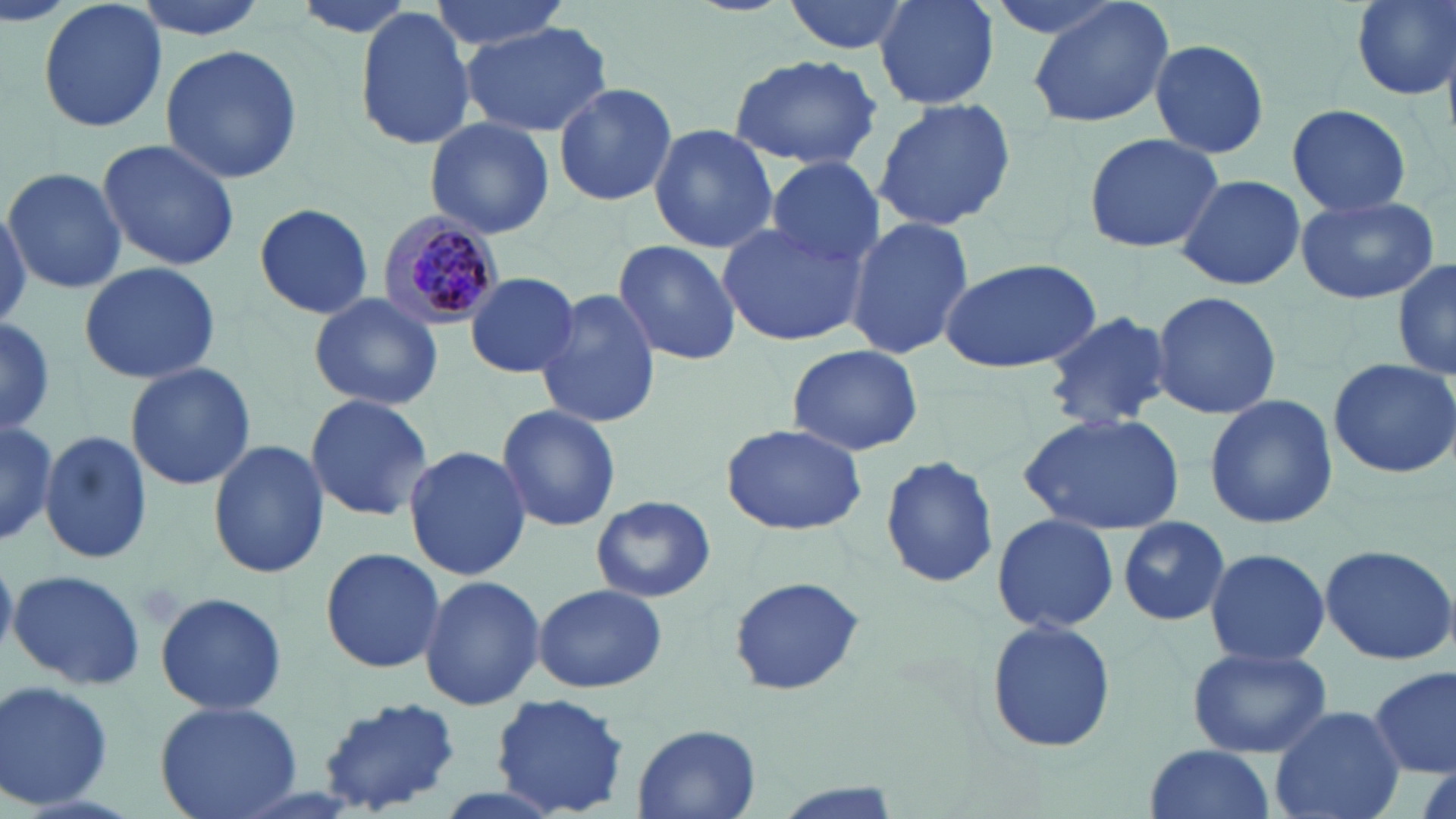
slide-level diagnosis = Plasmodium malariae
field of view = single
modality = optical microscopy
uninfected red blood cell locations = approximate bounding boxes as named x1/y1/x2/y2 corners in pixels: (x1=38, y1=0, x2=167, y2=133), (x1=128, y1=0, x2=272, y2=41), (x1=424, y1=0, x2=571, y2=51), (x1=784, y1=0, x2=912, y2=55), (x1=873, y1=0, x2=1000, y2=109), (x1=1027, y1=0, x2=1176, y2=131), (x1=1352, y1=0, x2=1455, y2=99), (x1=353, y1=9, x2=480, y2=149), (x1=461, y1=24, x2=612, y2=138), (x1=1147, y1=38, x2=1270, y2=159), (x1=159, y1=44, x2=304, y2=182), (x1=729, y1=53, x2=882, y2=170), (x1=551, y1=82, x2=678, y2=208), (x1=873, y1=97, x2=1017, y2=231), (x1=1284, y1=104, x2=1414, y2=218), (x1=424, y1=118, x2=555, y2=241), (x1=648, y1=123, x2=777, y2=252), (x1=1083, y1=131, x2=1225, y2=253), (x1=96, y1=137, x2=240, y2=272), (x1=764, y1=155, x2=883, y2=271), (x1=4, y1=168, x2=125, y2=293), (x1=1175, y1=174, x2=1306, y2=292), (x1=1296, y1=193, x2=1440, y2=305), (x1=0, y1=203, x2=31, y2=328), (x1=254, y1=203, x2=373, y2=319), (x1=845, y1=215, x2=974, y2=360), (x1=716, y1=220, x2=867, y2=348), (x1=613, y1=239, x2=740, y2=366), (x1=939, y1=256, x2=1101, y2=375), (x1=1393, y1=258, x2=1456, y2=383), (x1=77, y1=262, x2=222, y2=385), (x1=465, y1=272, x2=578, y2=377), (x1=535, y1=288, x2=664, y2=432), (x1=1150, y1=289, x2=1282, y2=421), (x1=308, y1=291, x2=445, y2=410), (x1=1043, y1=309, x2=1174, y2=429), (x1=0, y1=318, x2=59, y2=435), (x1=785, y1=345, x2=925, y2=457), (x1=1326, y1=357, x2=1456, y2=479), (x1=123, y1=361, x2=257, y2=491), (x1=1204, y1=392, x2=1339, y2=529), (x1=304, y1=393, x2=436, y2=521), (x1=496, y1=405, x2=622, y2=534), (x1=1021, y1=411, x2=1185, y2=534), (x1=719, y1=423, x2=870, y2=536), (x1=38, y1=428, x2=152, y2=569), (x1=207, y1=439, x2=328, y2=579), (x1=403, y1=445, x2=531, y2=581), (x1=879, y1=454, x2=1000, y2=589), (x1=590, y1=493, x2=715, y2=603), (x1=991, y1=512, x2=1119, y2=634), (x1=1116, y1=515, x2=1231, y2=628), (x1=1319, y1=543, x2=1456, y2=666), (x1=320, y1=546, x2=445, y2=674), (x1=1203, y1=547, x2=1330, y2=666), (x1=7, y1=568, x2=148, y2=691), (x1=418, y1=573, x2=546, y2=711), (x1=726, y1=577, x2=867, y2=698), (x1=532, y1=582, x2=667, y2=693), (x1=154, y1=591, x2=287, y2=717), (x1=985, y1=618, x2=1116, y2=755), (x1=1187, y1=646, x2=1331, y2=757), (x1=1369, y1=667, x2=1455, y2=778), (x1=0, y1=680, x2=116, y2=814), (x1=491, y1=693, x2=632, y2=817), (x1=316, y1=696, x2=464, y2=811), (x1=154, y1=701, x2=301, y2=819), (x1=1268, y1=704, x2=1408, y2=819), (x1=631, y1=724, x2=762, y2=817), (x1=1142, y1=744, x2=1276, y2=819)
image size = 1456×819 pixels
magnification = 1000x
stain = May-Grünwald-Giemsa
preparation = thin blood smear
Plasmodium malariae-infected red blood cell locations = approximate bounding boxes as named x1/y1/x2/y2 corners in pixels: (x1=381, y1=211, x2=505, y2=329)